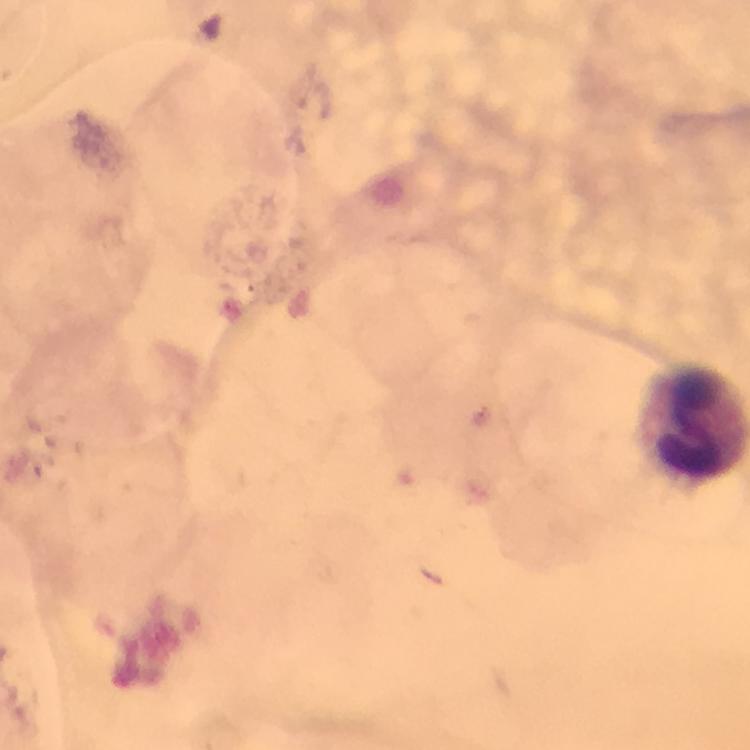

context: from a malaria diagnostic workup
preparation: thick blood film
cropped_from: a single field of view
leukocyte_locations: 'approximate centers as (x, y) in pixels: (695, 420)'
stain: Giemsa
capture: smartphone photograph through a microscope
image_size: 750×750 pixels
plasmodium_parasites: none seen
immersion_oil: used
magnification: 100x